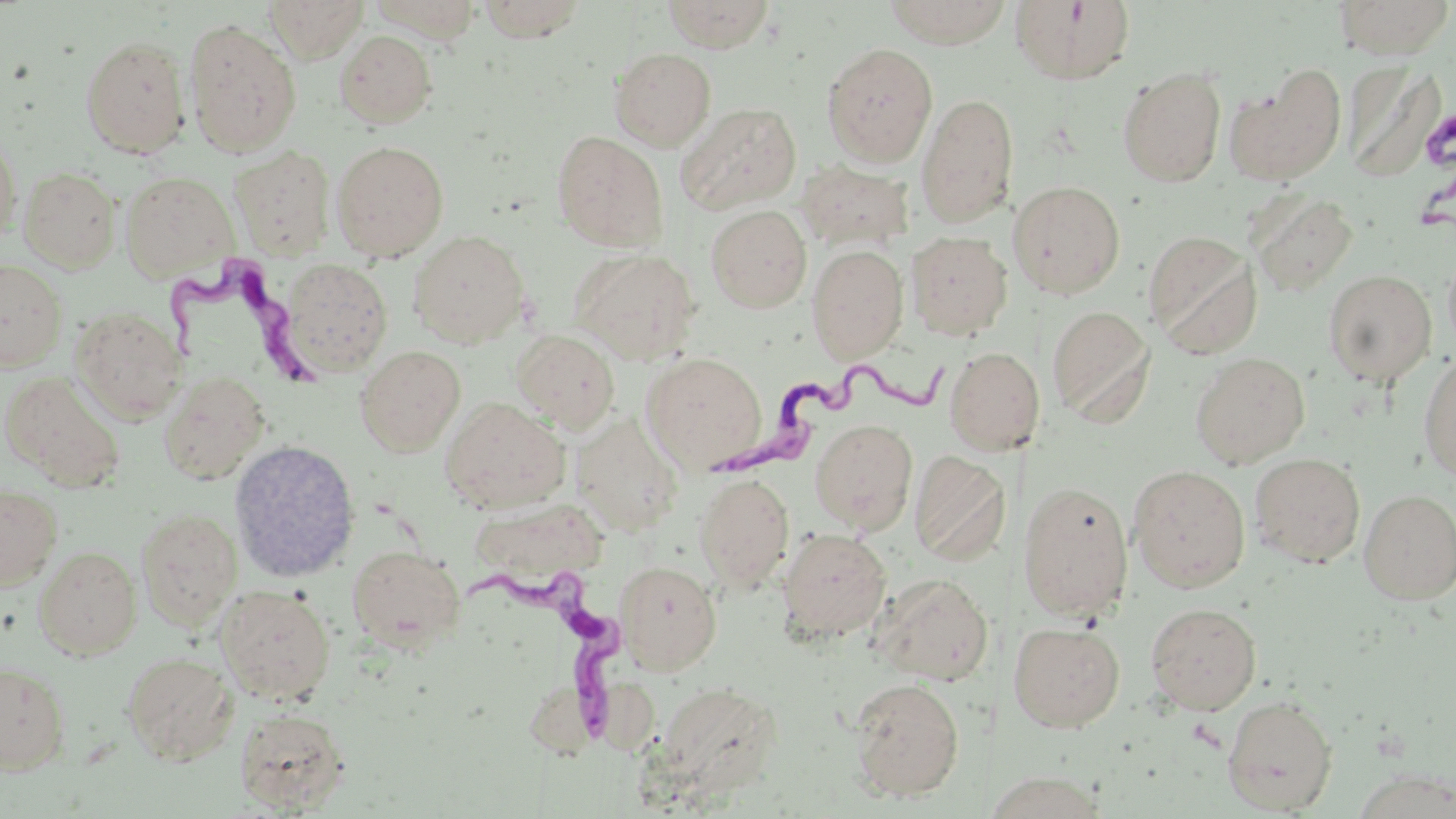
Summary:
  - Coordinate format: approximate bounding boxes as [x1, y1, x2, y2] in pixels
  - Trypanosoma brucei locations: [157, 261, 330, 403], [715, 356, 956, 481], [454, 564, 621, 742]
  - Uninfected red blood cell locations: [263, 0, 367, 62], [476, 0, 591, 43], [662, 0, 775, 52], [881, 0, 1013, 48], [1009, 0, 1137, 86], [1333, 0, 1455, 59], [183, 19, 302, 156], [335, 29, 438, 128], [79, 35, 191, 157], [821, 42, 938, 166], [609, 47, 716, 151], [1228, 66, 1346, 185], [1345, 66, 1443, 183], [1118, 67, 1226, 186], [917, 92, 1019, 225], [676, 102, 802, 214], [0, 130, 22, 244], [552, 130, 669, 253], [331, 140, 449, 261], [228, 145, 336, 260], [796, 161, 915, 251], [18, 166, 120, 272], [120, 171, 236, 280], [1009, 180, 1126, 300], [1247, 189, 1360, 298], [706, 204, 812, 312], [1144, 229, 1262, 359], [409, 230, 530, 347], [906, 231, 1012, 340], [807, 244, 909, 362], [570, 248, 701, 363], [1442, 248, 1456, 356], [0, 259, 67, 371], [281, 259, 393, 375], [1323, 270, 1438, 387], [1047, 305, 1155, 427], [70, 306, 185, 423], [511, 329, 620, 432], [355, 345, 466, 456], [945, 346, 1045, 454], [1418, 350, 1456, 483], [641, 352, 768, 472], [1190, 352, 1310, 468], [1, 370, 127, 490], [159, 370, 270, 484], [440, 398, 570, 512], [571, 413, 683, 535], [810, 418, 918, 534], [229, 439, 361, 582], [910, 450, 1010, 565], [1249, 453, 1366, 568], [1128, 464, 1250, 592], [695, 473, 795, 592], [1017, 480, 1134, 620], [0, 483, 63, 590], [1359, 489, 1456, 604], [461, 502, 614, 589], [136, 507, 242, 630], [778, 528, 892, 642], [347, 544, 464, 652], [33, 546, 142, 660], [615, 561, 721, 674], [872, 573, 994, 685], [216, 584, 336, 704], [1145, 602, 1261, 714], [1008, 621, 1125, 732], [122, 652, 237, 763], [0, 662, 70, 774], [849, 677, 965, 801], [655, 681, 783, 796], [1222, 695, 1338, 815], [234, 708, 349, 813], [981, 771, 1111, 817]
  - Slide-level diagnosis: Trypanosoma brucei
  - Image size: 1456×819 pixels
  - Preparation: thin blood film
  - Modality: light microscopy
  - Magnification: 1000x
  - Field of view: single
  - Stain: May-Grünwald-Giemsa